Report the malaria status of this cell.
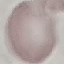
It is uninfected.

Summary:
  - Preparation: thin blood smear
  - Stain: Giemsa
  - Image type: automatically extracted cell patch, resized to 64 × 64 pixels
  - Capture: smartphone through the microscope eyepiece